Comment on the morphology of the erythrocytes.
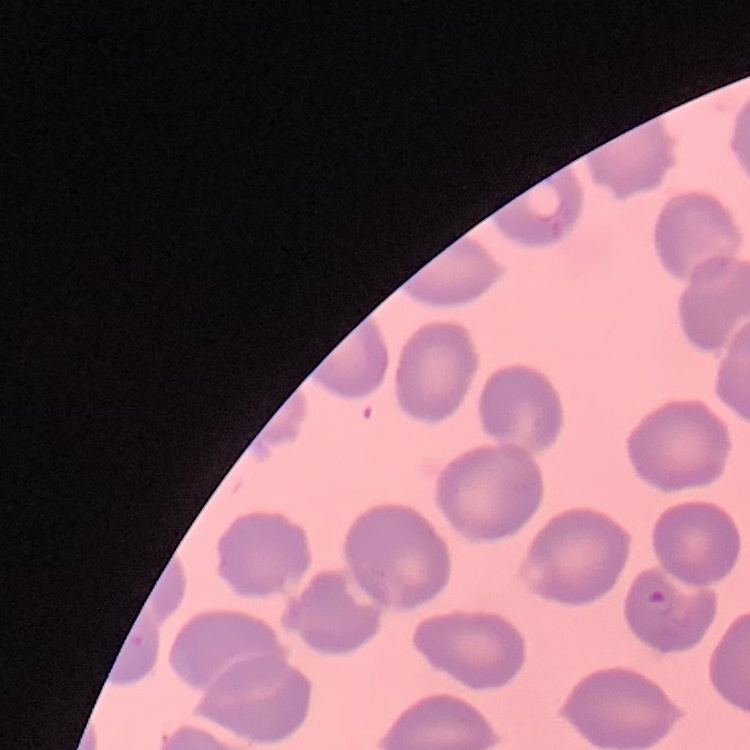

No rouleaux formation.

image_type: square crop of a larger photomicrograph
stain: Field's or Giemsa
preparation: thin blood film